Report the malaria status of this cell.
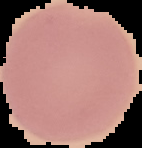
It is uninfected.

Segmented cell region on a black background. From a thin blood smear. Image is 142×148 pixels.